Report the malaria status of this cell.
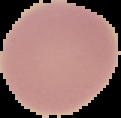
Uninfected.

Image is 121×118 pixels. The area outside the segmented cell region is set to black. From a thin blood film.